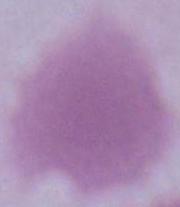

Photomicrograph. A red blood cell is shown. 1000x magnification.